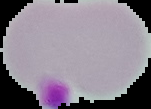
Malaria status: uninfected. Image is 151×109 pixels. From a thin blood smear. The area outside the segmented cell region is set to black.